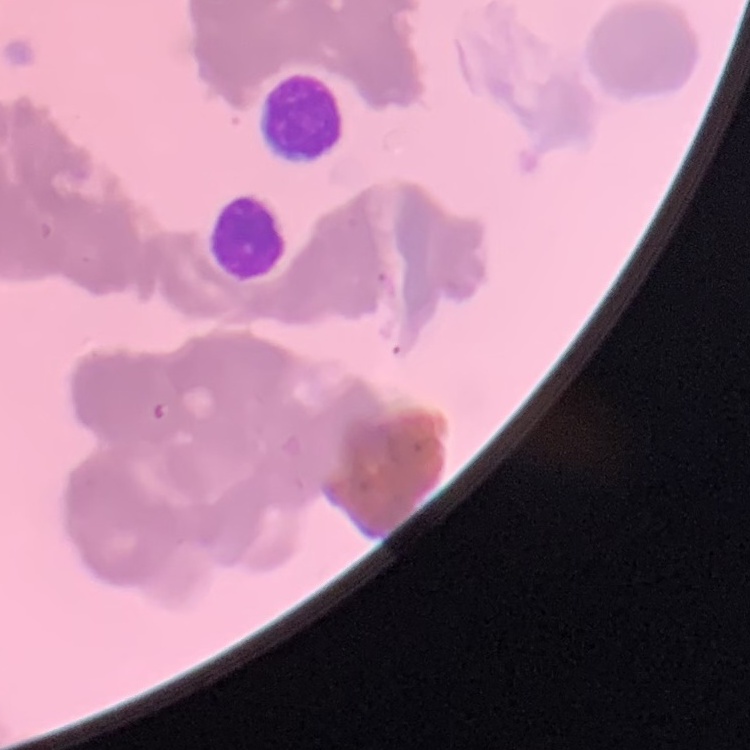
Summary:
  - Erythrocyte morphology: rouleaux formation
  - Stain: Field's or Giemsa
  - Preparation: thin peripheral smear
  - Image type: one tile cut from a larger photomicrograph